Identify the preparation type.
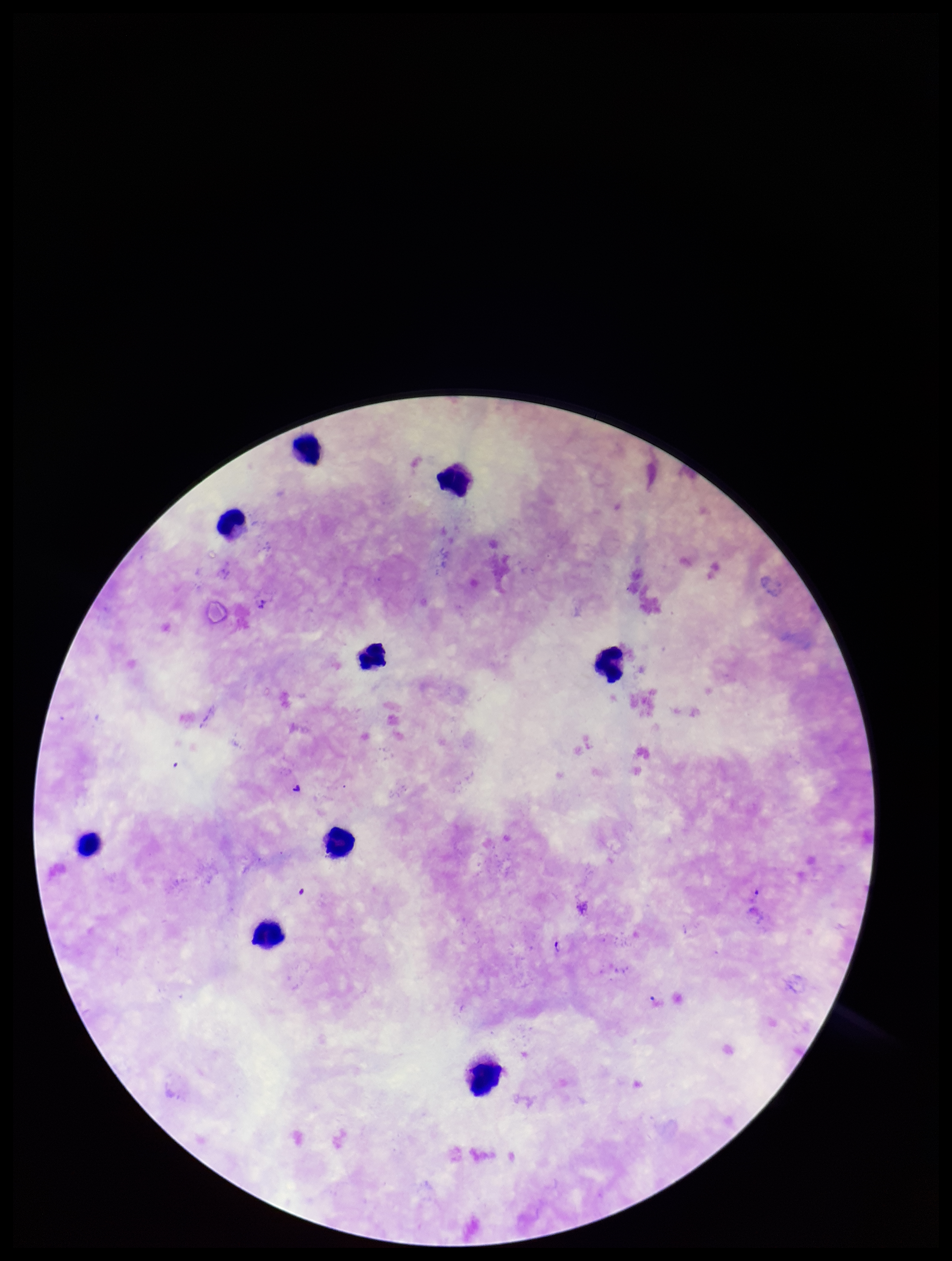
A thick smear.

species reported for this patient = Plasmodium falciparum
parasite count = 2
patient malaria status = infected
Plasmodium parasites = seen
stain = Giemsa
image size = 952×1261 pixels
capture = smartphone photograph through the microscope eyepiece
leukocyte count = 9
field of view = single